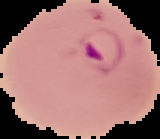

Cell region segmented out of the field of view; the surrounding area is masked to black. From a thin blood film. Image is 160×139 pixels. Result: Plasmodium parasites detected.